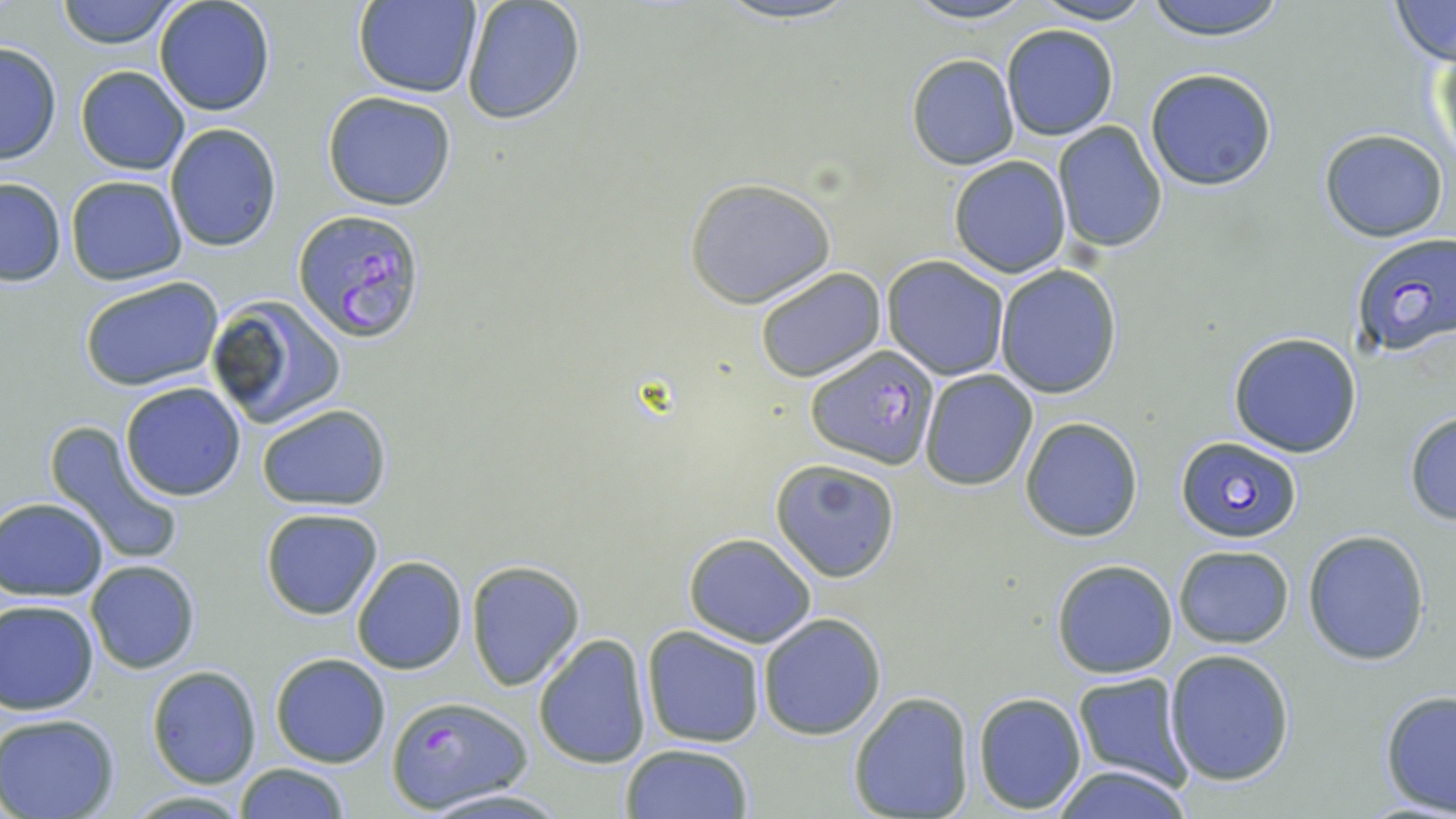
Summary:
  - Coordinate format: approximate bounding boxes as named x1/y1/x2/y2 corners in pixels
  - Uninfected red blood cell locations: (x1=53, y1=0, x2=184, y2=50), (x1=153, y1=0, x2=277, y2=117), (x1=707, y1=0, x2=868, y2=26), (x1=897, y1=0, x2=1045, y2=25), (x1=1142, y1=0, x2=1289, y2=41), (x1=355, y1=1, x2=481, y2=98), (x1=1033, y1=1, x2=1154, y2=25), (x1=1388, y1=1, x2=1455, y2=66), (x1=460, y1=2, x2=587, y2=126), (x1=1001, y1=23, x2=1119, y2=140), (x1=0, y1=41, x2=61, y2=166), (x1=1427, y1=47, x2=1455, y2=178), (x1=907, y1=54, x2=1019, y2=170), (x1=76, y1=65, x2=189, y2=174), (x1=1143, y1=67, x2=1278, y2=191), (x1=322, y1=92, x2=456, y2=210), (x1=164, y1=122, x2=282, y2=252), (x1=1051, y1=122, x2=1168, y2=253), (x1=1319, y1=129, x2=1450, y2=242), (x1=948, y1=155, x2=1070, y2=278), (x1=66, y1=174, x2=186, y2=283), (x1=0, y1=178, x2=67, y2=286), (x1=684, y1=178, x2=834, y2=308), (x1=882, y1=256, x2=1010, y2=381), (x1=994, y1=264, x2=1123, y2=399), (x1=754, y1=267, x2=886, y2=382), (x1=78, y1=275, x2=224, y2=393), (x1=207, y1=293, x2=349, y2=428), (x1=1228, y1=331, x2=1363, y2=458), (x1=919, y1=369, x2=1038, y2=491), (x1=119, y1=382, x2=247, y2=501), (x1=256, y1=403, x2=392, y2=511), (x1=1403, y1=410, x2=1456, y2=524), (x1=1020, y1=417, x2=1143, y2=541), (x1=42, y1=419, x2=185, y2=566), (x1=770, y1=458, x2=901, y2=583), (x1=1, y1=497, x2=109, y2=598), (x1=259, y1=506, x2=385, y2=621), (x1=1303, y1=528, x2=1431, y2=665), (x1=683, y1=532, x2=817, y2=647), (x1=1173, y1=544, x2=1294, y2=648), (x1=351, y1=556, x2=467, y2=674), (x1=1050, y1=559, x2=1179, y2=679), (x1=86, y1=560, x2=199, y2=675), (x1=466, y1=562, x2=585, y2=691), (x1=1, y1=599, x2=100, y2=716), (x1=758, y1=612, x2=888, y2=741), (x1=641, y1=627, x2=765, y2=748), (x1=532, y1=634, x2=652, y2=769), (x1=1165, y1=649, x2=1295, y2=784), (x1=270, y1=653, x2=391, y2=768), (x1=147, y1=666, x2=262, y2=788), (x1=1071, y1=671, x2=1191, y2=790), (x1=1379, y1=690, x2=1456, y2=814), (x1=847, y1=692, x2=975, y2=819), (x1=973, y1=692, x2=1087, y2=812), (x1=0, y1=712, x2=121, y2=819), (x1=620, y1=743, x2=755, y2=819), (x1=235, y1=763, x2=349, y2=818), (x1=1046, y1=764, x2=1194, y2=819), (x1=418, y1=789, x2=571, y2=817), (x1=124, y1=791, x2=254, y2=818)
  - Plasmodium falciparum-infected red blood cell locations: (x1=292, y1=206, x2=427, y2=345), (x1=1346, y1=234, x2=1455, y2=358), (x1=806, y1=342, x2=938, y2=468), (x1=1175, y1=435, x2=1302, y2=543), (x1=386, y1=695, x2=531, y2=812)
  - Slide-level diagnosis: Plasmodium falciparum
  - Modality: light microscopy
  - Preparation: thin blood film
  - Field of view: single
  - Image size: 1456×819 pixels
  - Stain: May-Grünwald-Giemsa
  - Magnification: 1000x